Describe the morphology of the erythrocytes.
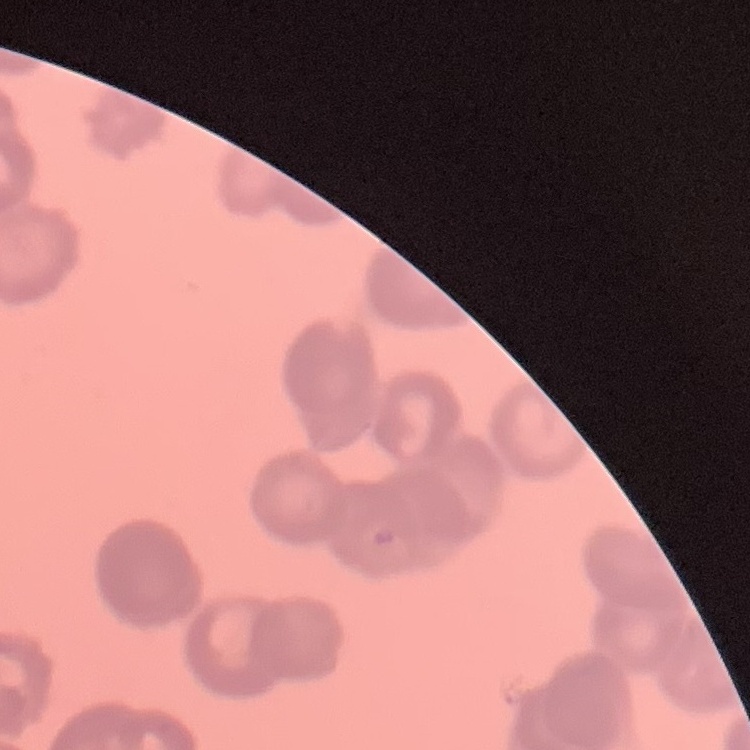
Rouleaux formation.

image type = square crop of a larger photomicrograph
preparation = thin blood smear
stain = Field's or Giemsa